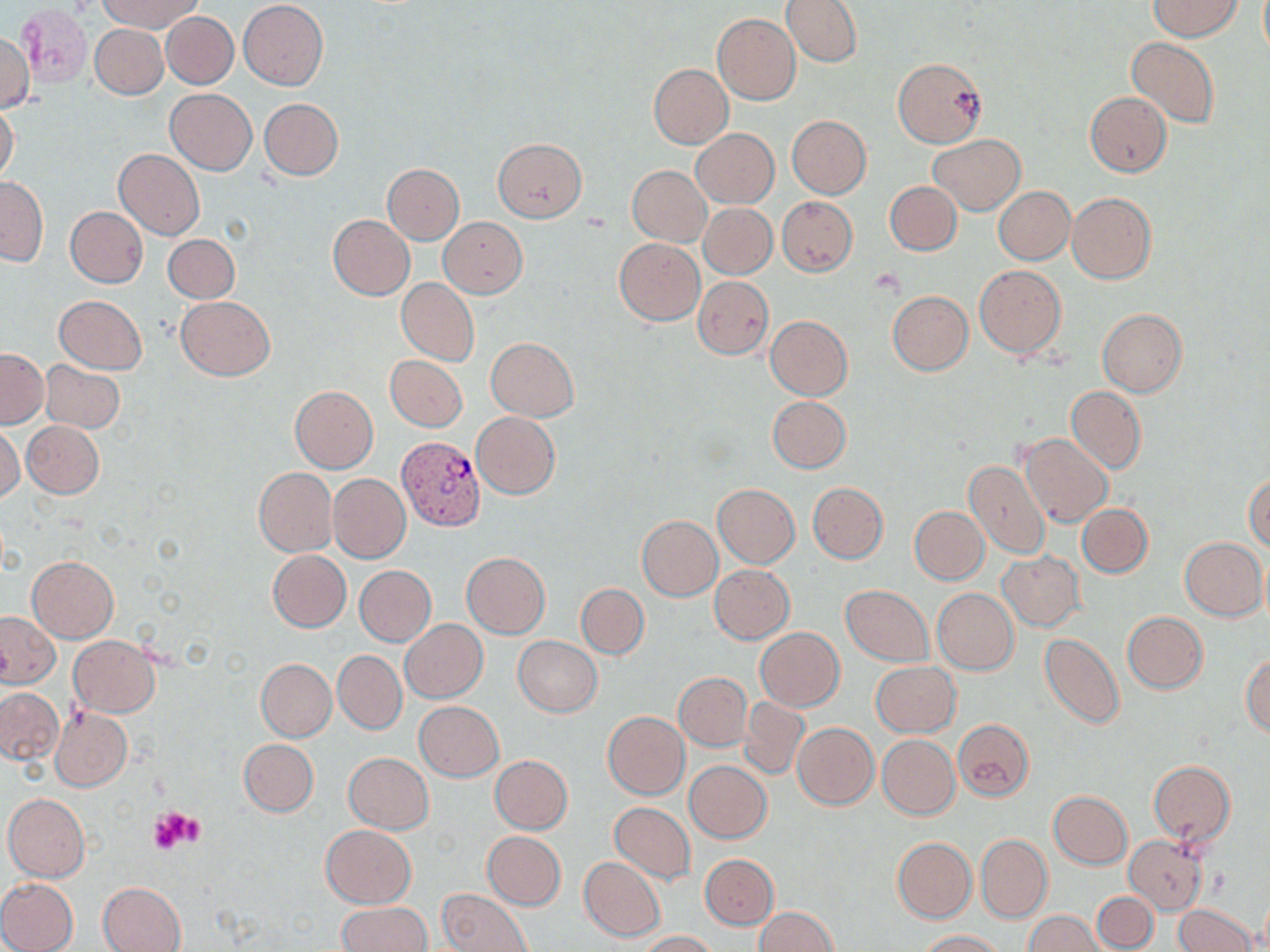
slide-level diagnosis = Plasmodium vivax
stain = May-Grünwald-Giemsa
magnification = 1000x
preparation = thin blood film
field of view = single
image size = 1270×952 pixels
platelet locations = approximate bounding boxes as named x1/y1/x2/y2 corners in pixels: (x1=150, y1=806, x2=206, y2=854)
modality = optical microscopy
Plasmodium vivax-infected red blood cell locations = approximate bounding boxes as named x1/y1/x2/y2 corners in pixels: (x1=395, y1=437, x2=484, y2=534)
uninfected red blood cell locations = approximate bounding boxes as named x1/y1/x2/y2 corners in pixels: (x1=96, y1=0, x2=204, y2=32), (x1=239, y1=0, x2=328, y2=90), (x1=782, y1=0, x2=862, y2=67), (x1=1148, y1=0, x2=1242, y2=40), (x1=18, y1=5, x2=93, y2=87), (x1=162, y1=12, x2=239, y2=88), (x1=711, y1=13, x2=801, y2=105), (x1=90, y1=24, x2=168, y2=98), (x1=0, y1=29, x2=34, y2=113), (x1=1127, y1=37, x2=1218, y2=128), (x1=893, y1=57, x2=986, y2=147), (x1=648, y1=64, x2=733, y2=149), (x1=166, y1=89, x2=257, y2=175), (x1=1085, y1=91, x2=1172, y2=177), (x1=259, y1=98, x2=344, y2=180), (x1=0, y1=100, x2=20, y2=184), (x1=787, y1=115, x2=872, y2=198), (x1=691, y1=128, x2=778, y2=208), (x1=929, y1=134, x2=1026, y2=214), (x1=493, y1=137, x2=587, y2=222), (x1=115, y1=148, x2=204, y2=240), (x1=383, y1=163, x2=464, y2=244), (x1=628, y1=166, x2=710, y2=246), (x1=1, y1=177, x2=48, y2=266), (x1=885, y1=181, x2=962, y2=255), (x1=994, y1=186, x2=1075, y2=263), (x1=1066, y1=192, x2=1156, y2=284), (x1=777, y1=196, x2=856, y2=276), (x1=699, y1=203, x2=776, y2=279), (x1=65, y1=207, x2=147, y2=288), (x1=328, y1=215, x2=414, y2=299), (x1=438, y1=217, x2=527, y2=298), (x1=164, y1=233, x2=239, y2=303), (x1=614, y1=238, x2=705, y2=325), (x1=974, y1=264, x2=1066, y2=358), (x1=692, y1=275, x2=773, y2=359), (x1=396, y1=278, x2=479, y2=366), (x1=887, y1=291, x2=973, y2=375), (x1=54, y1=295, x2=146, y2=374), (x1=177, y1=295, x2=276, y2=380), (x1=1098, y1=308, x2=1187, y2=397), (x1=765, y1=316, x2=853, y2=400), (x1=485, y1=337, x2=579, y2=420), (x1=0, y1=348, x2=48, y2=428), (x1=386, y1=355, x2=467, y2=432), (x1=40, y1=360, x2=125, y2=435), (x1=290, y1=386, x2=378, y2=473), (x1=1066, y1=386, x2=1146, y2=474), (x1=767, y1=396, x2=851, y2=473), (x1=470, y1=412, x2=560, y2=499), (x1=22, y1=420, x2=104, y2=498), (x1=0, y1=424, x2=24, y2=503), (x1=1021, y1=433, x2=1112, y2=528), (x1=963, y1=461, x2=1050, y2=562), (x1=253, y1=468, x2=338, y2=558), (x1=1244, y1=472, x2=1270, y2=552), (x1=328, y1=474, x2=410, y2=563), (x1=807, y1=482, x2=888, y2=563), (x1=712, y1=484, x2=800, y2=569), (x1=1076, y1=503, x2=1153, y2=578), (x1=909, y1=506, x2=989, y2=584), (x1=637, y1=516, x2=722, y2=601), (x1=1180, y1=537, x2=1268, y2=620), (x1=267, y1=550, x2=351, y2=631), (x1=998, y1=550, x2=1086, y2=632), (x1=461, y1=553, x2=550, y2=639), (x1=1260, y1=554, x2=1270, y2=632), (x1=27, y1=556, x2=118, y2=642), (x1=709, y1=565, x2=795, y2=643), (x1=355, y1=566, x2=435, y2=646), (x1=576, y1=584, x2=649, y2=658), (x1=840, y1=585, x2=934, y2=665), (x1=931, y1=588, x2=1019, y2=675), (x1=1, y1=611, x2=60, y2=688), (x1=1122, y1=612, x2=1208, y2=693), (x1=400, y1=619, x2=488, y2=703), (x1=754, y1=627, x2=844, y2=711), (x1=1040, y1=634, x2=1124, y2=729), (x1=69, y1=635, x2=161, y2=717), (x1=514, y1=636, x2=602, y2=717), (x1=333, y1=650, x2=407, y2=734), (x1=1242, y1=655, x2=1270, y2=737), (x1=255, y1=659, x2=336, y2=741), (x1=870, y1=661, x2=961, y2=736), (x1=674, y1=672, x2=751, y2=751), (x1=0, y1=688, x2=63, y2=764), (x1=740, y1=697, x2=811, y2=779), (x1=414, y1=701, x2=504, y2=781), (x1=51, y1=707, x2=131, y2=791), (x1=603, y1=712, x2=688, y2=799), (x1=953, y1=719, x2=1035, y2=800), (x1=792, y1=722, x2=879, y2=809), (x1=877, y1=735, x2=959, y2=819), (x1=239, y1=739, x2=318, y2=816), (x1=343, y1=753, x2=433, y2=833), (x1=489, y1=755, x2=573, y2=833), (x1=684, y1=761, x2=772, y2=843), (x1=1148, y1=761, x2=1237, y2=844), (x1=1048, y1=790, x2=1132, y2=869), (x1=3, y1=793, x2=90, y2=882), (x1=609, y1=802, x2=695, y2=883), (x1=321, y1=825, x2=416, y2=908), (x1=482, y1=831, x2=566, y2=910), (x1=976, y1=833, x2=1052, y2=923), (x1=1125, y1=835, x2=1208, y2=914), (x1=892, y1=837, x2=976, y2=923), (x1=701, y1=853, x2=778, y2=929), (x1=579, y1=857, x2=666, y2=942), (x1=0, y1=877, x2=79, y2=952), (x1=98, y1=881, x2=187, y2=952), (x1=438, y1=889, x2=532, y2=952), (x1=1092, y1=892, x2=1158, y2=951), (x1=337, y1=902, x2=431, y2=951), (x1=1174, y1=903, x2=1255, y2=952), (x1=755, y1=906, x2=840, y2=951), (x1=1024, y1=910, x2=1106, y2=951), (x1=638, y1=930, x2=718, y2=951), (x1=917, y1=930, x2=1005, y2=951)